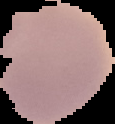
image type = segmented cell region on a black background
preparation = thin blood smear
result = no malaria parasites seen
image size = 115×124 pixels